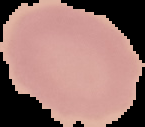 From a thin blood film. Segmented cell region on a black background. Result: negative for Plasmodium parasites. Image is 145×127 pixels.